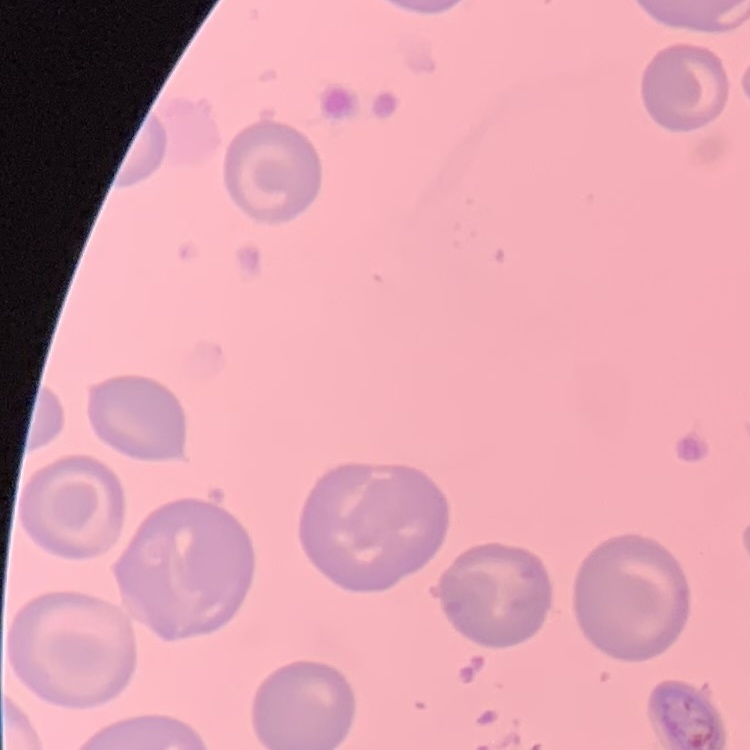

The erythrocytes show no rouleaux formation. Field's or Giemsa stain. Thin blood film. One tile cut from a larger photomicrograph.